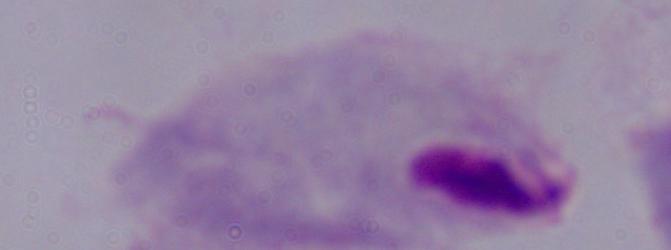

modality = photomicrograph
magnification = 1000x
identification = trichomonad